Assess the morphology of the red blood cells.
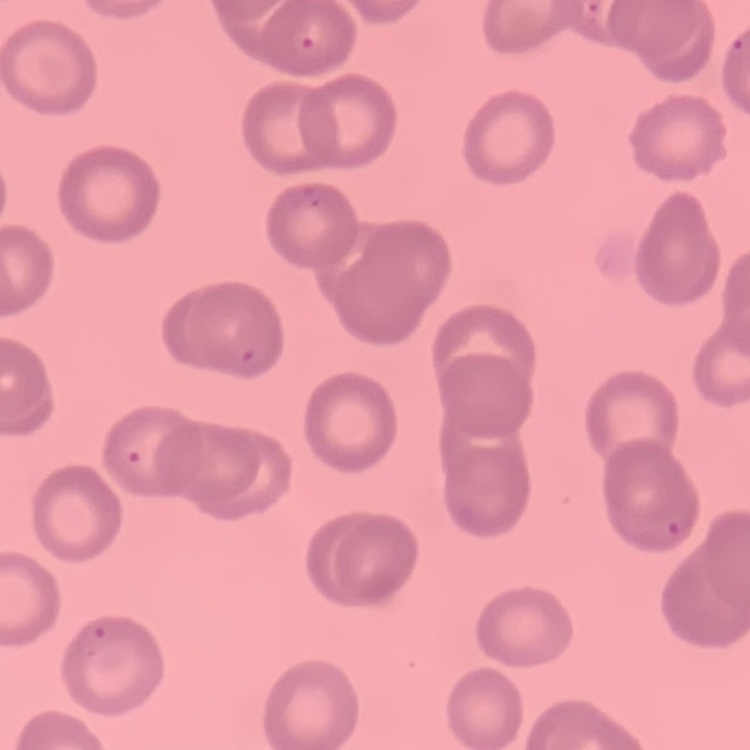
No rouleaux formation.

Field's or Giemsa stain. Square crop of a larger photomicrograph. Thin blood smear.